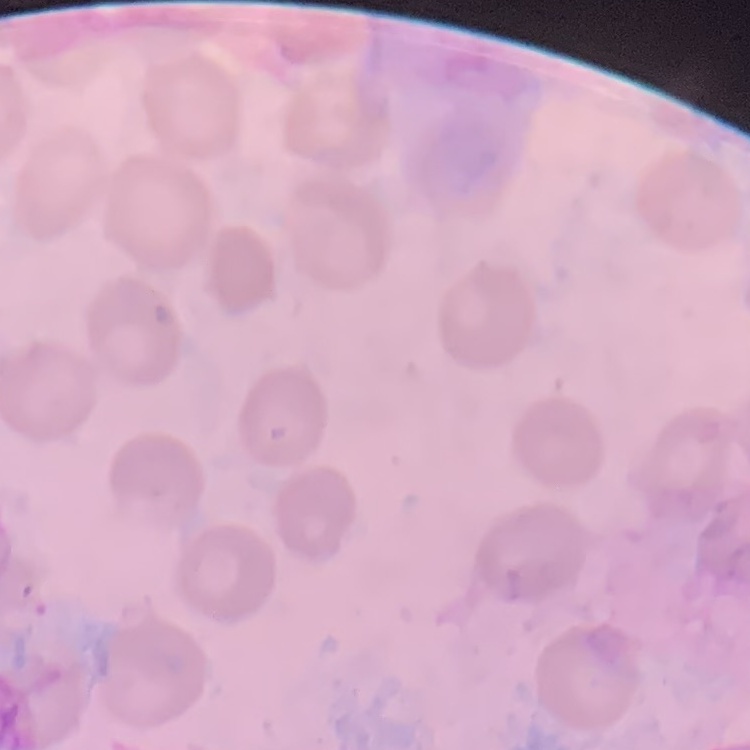
The erythrocytes exhibit no rouleaux formation. Thin peripheral smear. One tile cut from a larger photomicrograph. Field's or Giemsa stain.